Name the blood parasite species.
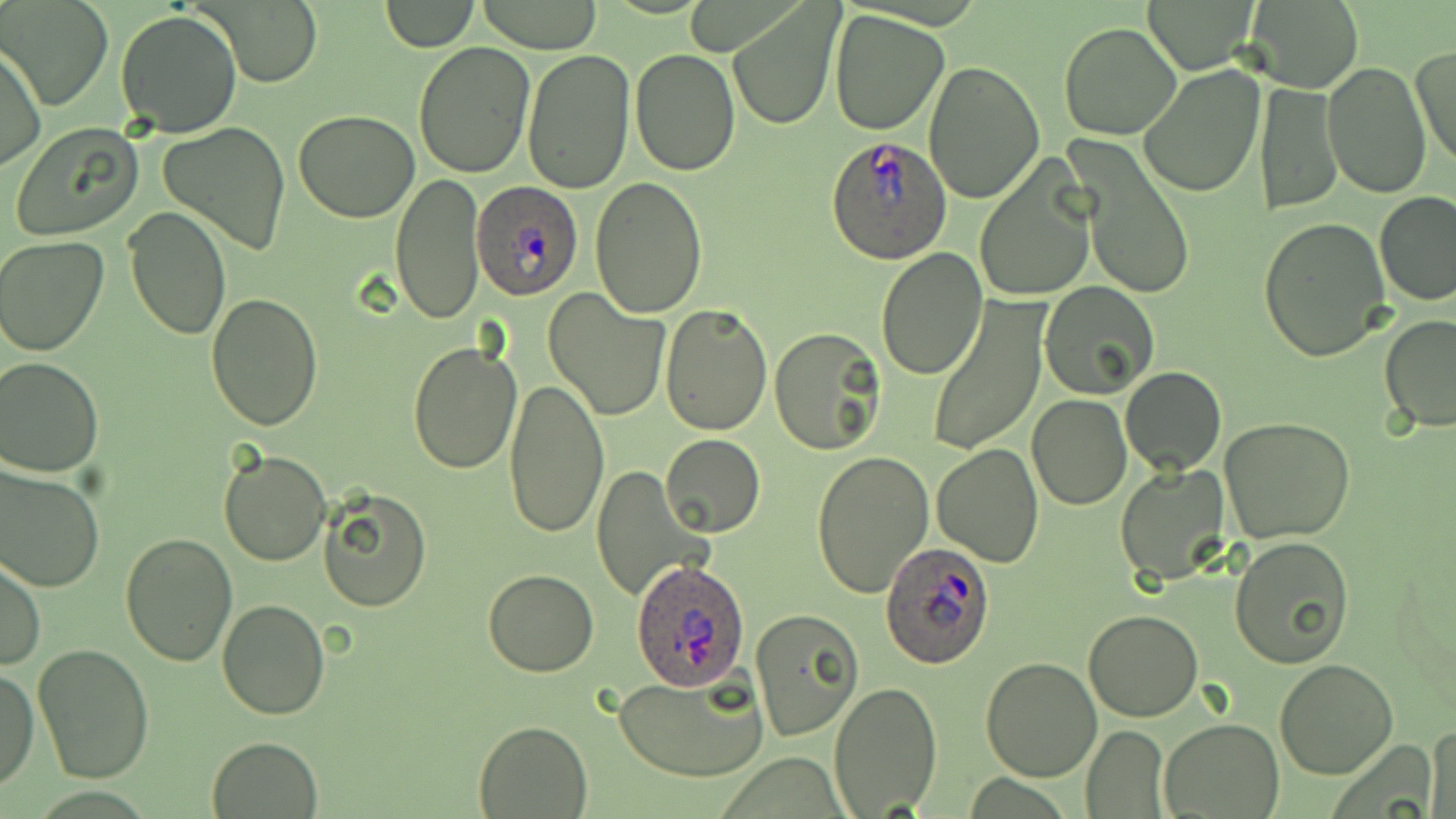

Plasmodium ovale.

Summary:
  - Coordinate format: approximate bounding boxes as (x1,y1)-(x2,y2) corner pairs in pixels
  - Plasmodium ovale-infected red blood cell locations: (824,136)-(950,265), (472,181)-(584,301), (880,542)-(994,668), (626,559)-(752,693)
  - Uninfected red blood cell locations: (1143,0)-(1260,73), (1240,0)-(1366,93), (476,1)-(603,53), (6,2)-(111,109), (202,2)-(322,86), (379,2)-(479,52), (727,2)-(842,132), (114,9)-(243,138), (828,10)-(949,135), (1058,22)-(1182,140), (412,41)-(536,178), (1,43)-(45,174), (1409,43)-(1455,172), (630,47)-(740,176), (520,48)-(635,195), (922,60)-(1045,205), (1323,62)-(1431,200), (1139,63)-(1266,198), (1257,81)-(1342,214), (293,110)-(421,222), (9,122)-(144,241), (158,122)-(291,256), (1066,138)-(1195,303), (974,160)-(1097,302), (391,173)-(486,325), (589,178)-(709,319), (1375,193)-(1456,305), (123,204)-(231,341), (1258,216)-(1392,362), (1,236)-(108,356), (876,248)-(988,379), (1040,283)-(1162,400), (542,291)-(671,423), (206,293)-(324,431), (925,299)-(1048,458), (660,304)-(771,435), (1379,315)-(1456,433), (768,329)-(885,456), (407,341)-(521,475), (0,357)-(104,475), (1119,365)-(1225,475), (503,376)-(608,537), (1027,395)-(1132,510), (1219,417)-(1355,543), (661,435)-(765,537), (932,444)-(1042,566), (218,448)-(332,566), (809,449)-(934,601), (0,463)-(105,592), (1116,464)-(1229,587), (590,465)-(714,606), (319,490)-(431,612), (118,530)-(237,667), (1229,535)-(1356,668), (0,556)-(44,671), (481,568)-(600,677), (217,599)-(330,721), (1083,609)-(1202,722), (750,610)-(863,742), (33,642)-(157,782), (980,657)-(1102,782), (1273,658)-(1397,779), (0,665)-(39,793), (612,668)-(768,783), (829,682)-(943,817), (1161,718)-(1283,818), (474,720)-(593,818), (1080,724)-(1169,817), (1427,728)-(1455,819), (207,735)-(323,818)
  - Stain: May-Grünwald-Giemsa
  - Magnification: 1000x
  - Image size: 1456×819 pixels
  - Preparation: thin blood smear
  - Modality: optical microscopy
  - Field of view: single